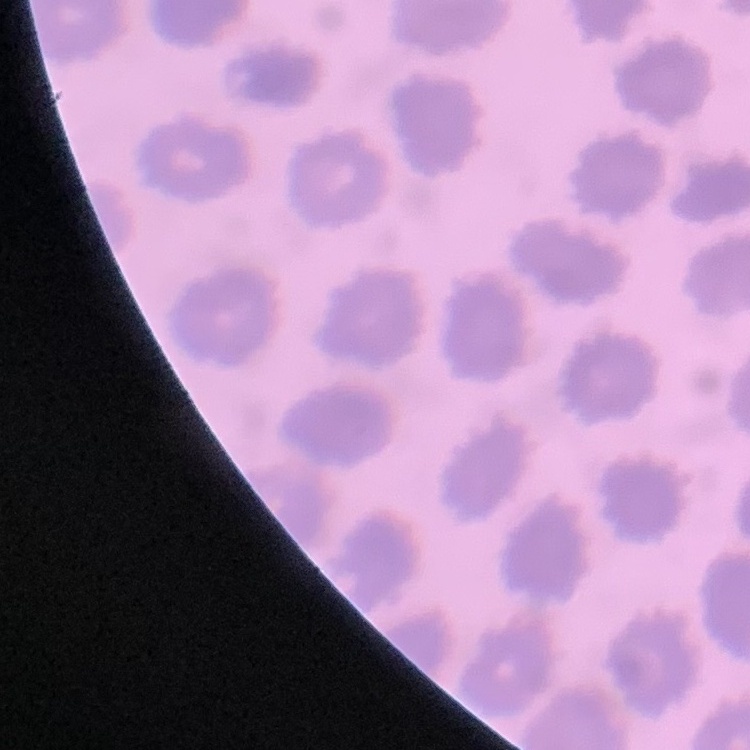
The erythrocytes show no rouleaux formation. Thin peripheral smear. Square crop of a larger photomicrograph. Stained with either Field's or Giemsa.